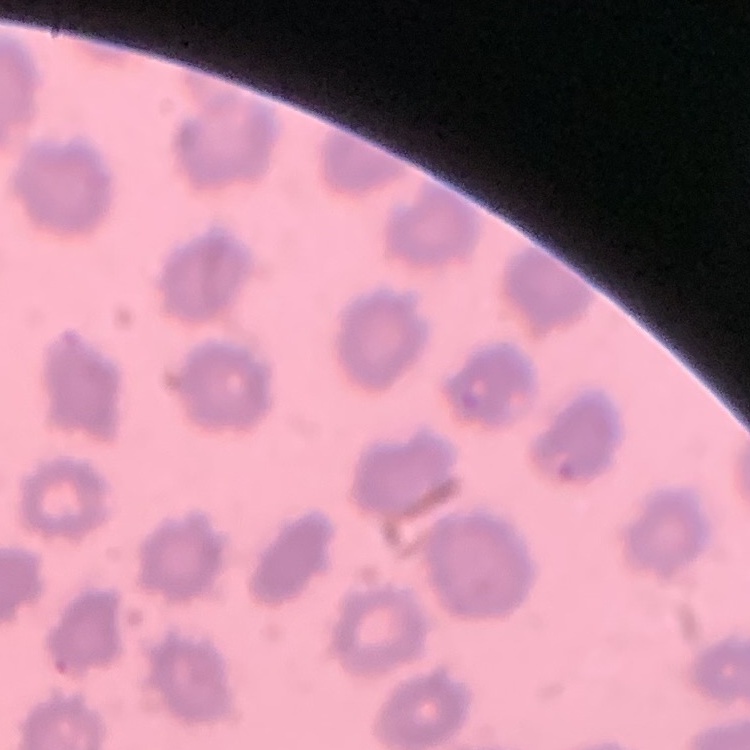 The erythrocytes exhibit no rouleaux formation. Square crop of a larger photomicrograph. Thin blood smear. Stained with either Field's or Giemsa.